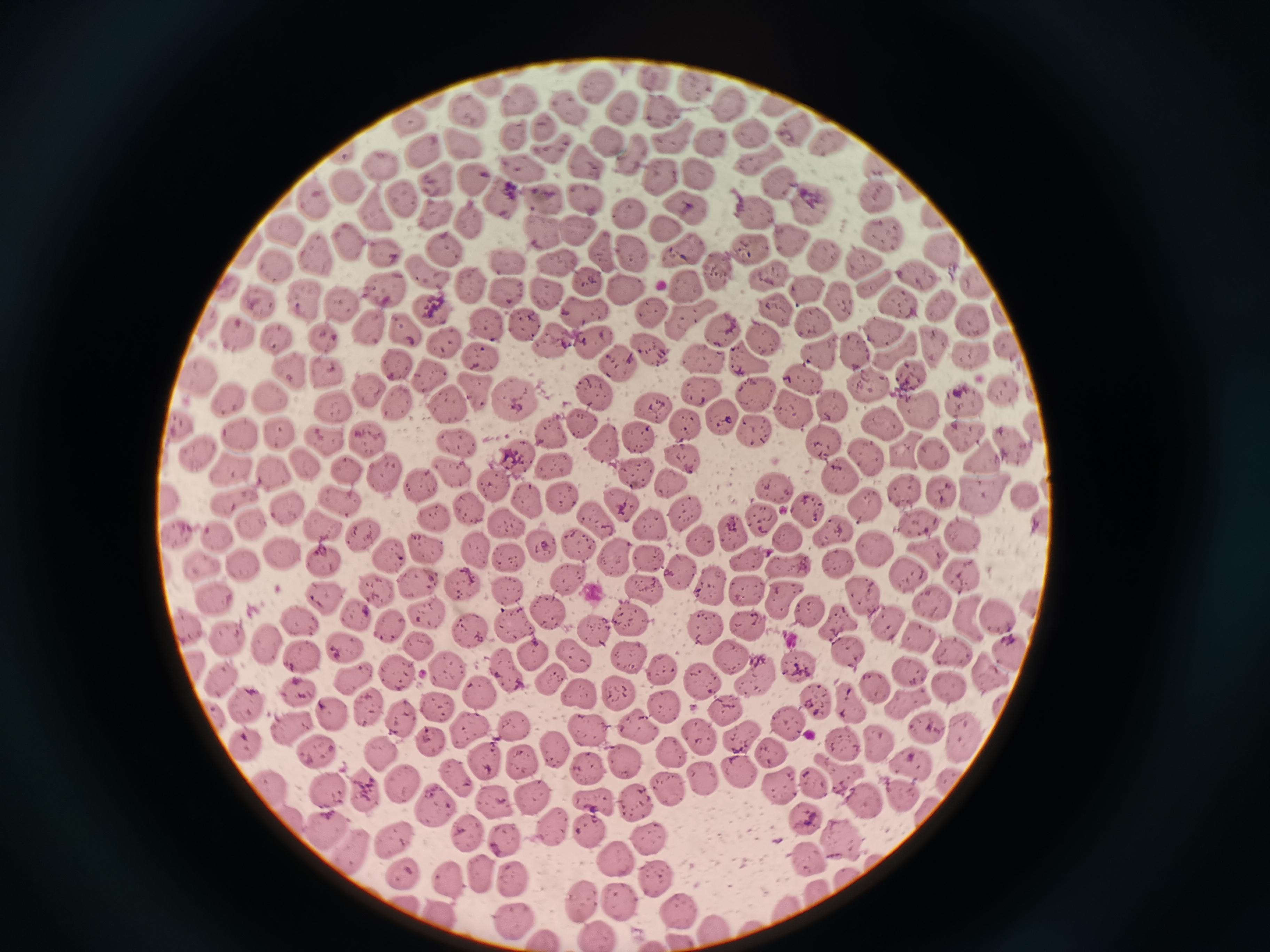
Approximate centers as [x, y] in pixels. Cell locations: [658, 79], [598, 85], [695, 85], [523, 100], [782, 103], [570, 105], [627, 105], [733, 106], [472, 110], [664, 110], [416, 119], [544, 123], [513, 130], [798, 130], [753, 134], [676, 135], [610, 142], [461, 143], [835, 143], [715, 145], [556, 148], [420, 149], [640, 153], [762, 158], [589, 160], [381, 167], [883, 169], [525, 172], [701, 175], [435, 177], [665, 178], [785, 180], [475, 184], [352, 189], [911, 189], [403, 193], [501, 193], [586, 196], [879, 197], [542, 199], [317, 201], [814, 204], [688, 209], [755, 211], [434, 214], [631, 215], [936, 215], [378, 216], [469, 220], [540, 227], [664, 227], [286, 231], [576, 232], [886, 233], [791, 239], [347, 240], [754, 247], [442, 248], [604, 251], [317, 252], [382, 252], [637, 252], [944, 252], [825, 253], [687, 254], [507, 261], [556, 262], [864, 262], [280, 265], [722, 266], [916, 269], [424, 271], [771, 272], [472, 281], [589, 284], [688, 285], [386, 286], [809, 289], [878, 289], [507, 292], [627, 293], [547, 294], [305, 295], [841, 298], [261, 299], [343, 300], [778, 304], [947, 304], [902, 305], [584, 309], [434, 310], [652, 313], [815, 319], [692, 321], [488, 323], [973, 324], [366, 325], [721, 325], [403, 327], [525, 327], [240, 331], [881, 331], [325, 334], [276, 336], [763, 339], [556, 341], [595, 341], [447, 343], [935, 345], [858, 347], [650, 349], [820, 349], [972, 351], [481, 352], [750, 359], [703, 360], [401, 362], [621, 363], [291, 367], [328, 372], [427, 374], [803, 376], [914, 377], [204, 379], [870, 386], [365, 389], [475, 389], [1004, 390], [702, 391], [595, 394], [271, 395], [755, 396], [234, 400], [512, 400], [963, 401], [395, 404], [449, 405], [831, 406], [335, 407], [790, 409], [649, 410], [917, 411], [719, 414], [583, 420], [884, 424], [687, 425], [181, 428], [550, 430], [752, 430], [282, 433], [240, 434], [965, 434], [323, 437], [365, 437], [639, 438], [457, 440], [824, 440], [1011, 440], [605, 442], [197, 452], [908, 452], [936, 455], [682, 458], [866, 458], [516, 460], [990, 461], [305, 464], [551, 465], [277, 468], [229, 469], [451, 469], [349, 470], [384, 473], [840, 473], [638, 476], [492, 481], [421, 483], [671, 484], [774, 485], [904, 487], [942, 492], [563, 493], [983, 494], [1023, 494], [166, 498], [234, 498], [343, 499], [528, 499], [617, 500], [867, 504], [288, 508], [475, 508], [805, 510], [684, 512], [436, 515], [763, 517], [509, 521], [595, 521], [916, 522], [251, 523], [326, 525], [652, 525], [832, 526], [733, 531], [361, 533], [789, 533], [216, 535], [178, 536], [964, 537], [702, 541], [424, 546], [542, 546], [577, 546], [479, 549], [877, 549], [279, 552], [386, 554], [647, 554], [932, 554], [509, 557], [322, 558], [618, 558], [838, 561], [749, 562], [204, 563], [790, 563], [243, 566], [679, 570], [906, 571], [960, 577], [571, 578], [462, 579], [420, 583], [641, 585], [709, 585], [376, 589], [505, 589], [746, 592], [214, 593], [861, 594], [327, 597], [786, 597], [932, 604], [809, 612], [547, 613], [427, 614], [997, 615], [635, 617], [971, 618], [301, 621], [840, 622], [705, 624], [889, 624], [389, 625], [189, 626], [511, 626], [748, 626], [469, 629], [591, 629], [232, 638], [922, 641], [271, 642], [420, 645], [846, 646], [1008, 647], [343, 650], [953, 650], [532, 651], [570, 651], [628, 656], [304, 657], [731, 657], [797, 663], [446, 668], [505, 668], [661, 669], [400, 670], [909, 670], [985, 672], [701, 676], [220, 677], [761, 677], [547, 679], [355, 681], [872, 684], [948, 686], [297, 689], [622, 689], [575, 692], [486, 694], [848, 698], [815, 699], [908, 699], [664, 704], [241, 705], [440, 705], [369, 709], [727, 710], [329, 712], [401, 716], [790, 723], [511, 726], [289, 727], [926, 727], [584, 728], [636, 728], [469, 733], [961, 734], [692, 736], [243, 739], [430, 739], [880, 739], [740, 741], [844, 742], [553, 743], [317, 750], [769, 750], [668, 751], [381, 754], [624, 761], [485, 762], [524, 762], [911, 765], [590, 768], [736, 771], [840, 772], [453, 775], [701, 777], [950, 780], [811, 781], [664, 783], [405, 785], [783, 786], [328, 788], [274, 790], [365, 791], [901, 793], [535, 796], [635, 796], [866, 799], [594, 800], [501, 806], [435, 808], [931, 811], [805, 816], [552, 824], [467, 830], [327, 831], [594, 832], [507, 835], [646, 837], [395, 838], [840, 841], [350, 852], [807, 855], [617, 862], [403, 869], [479, 870], [656, 874], [448, 876], [513, 878], [580, 896], [615, 897], [681, 910], [515, 918], [597, 930]. Thin blood smear. Giemsa-stained preparation. Image is 1270×952 pixels. Single field of view. Photographed with a smartphone camera at the microscope eyepiece.